Report the malaria status of this cell.
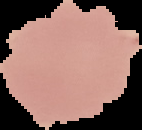

Uninfected.

Summary:
  - Preparation: thin blood film
  - Image size: 142×130 pixels
  - Image type: segmented cell region on a black background